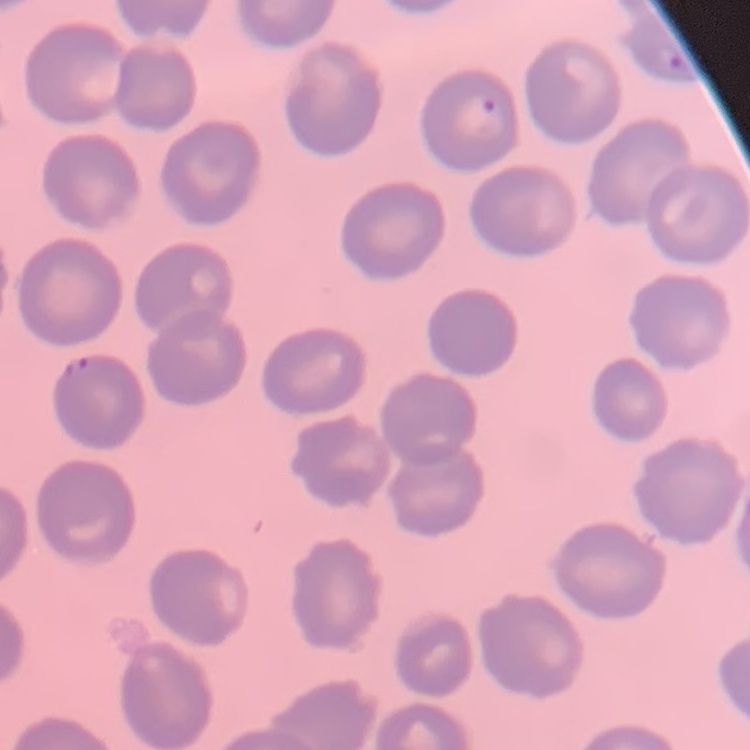
{
  "red_blood_cell_morphology": "no rouleaux formation",
  "image_type": "one tile cut from a larger photomicrograph",
  "preparation": "thin blood smear",
  "stain": "Field's or Giemsa"
}